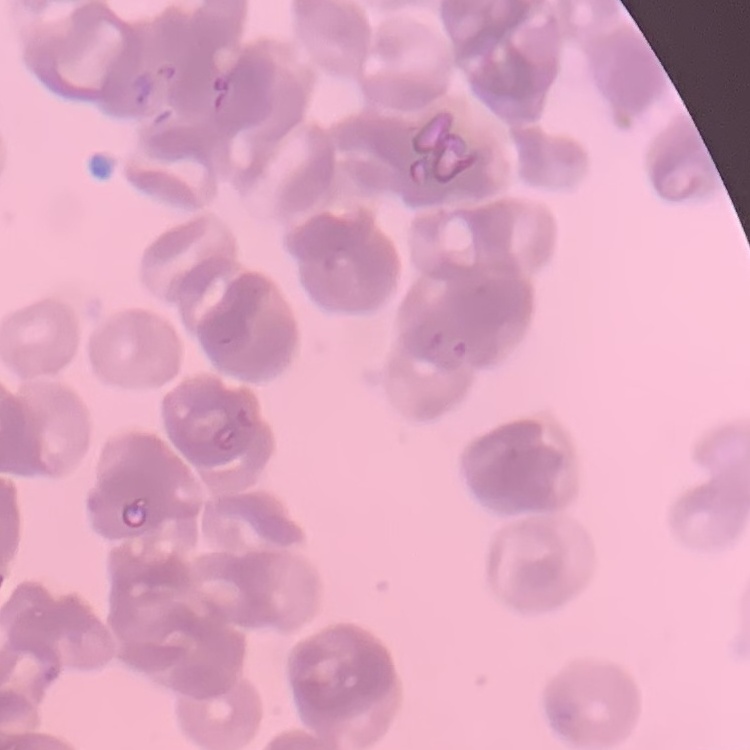
Summary:
  - Erythrocyte morphology: rouleaux formation
  - Stain: Field's or Giemsa
  - Image type: one tile cut from a larger photomicrograph
  - Preparation: thin blood film